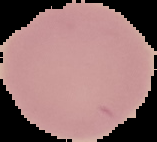
Image is 157×142 pixels. Segmented cell region on a black background. Malaria status: uninfected. From a thin blood smear.